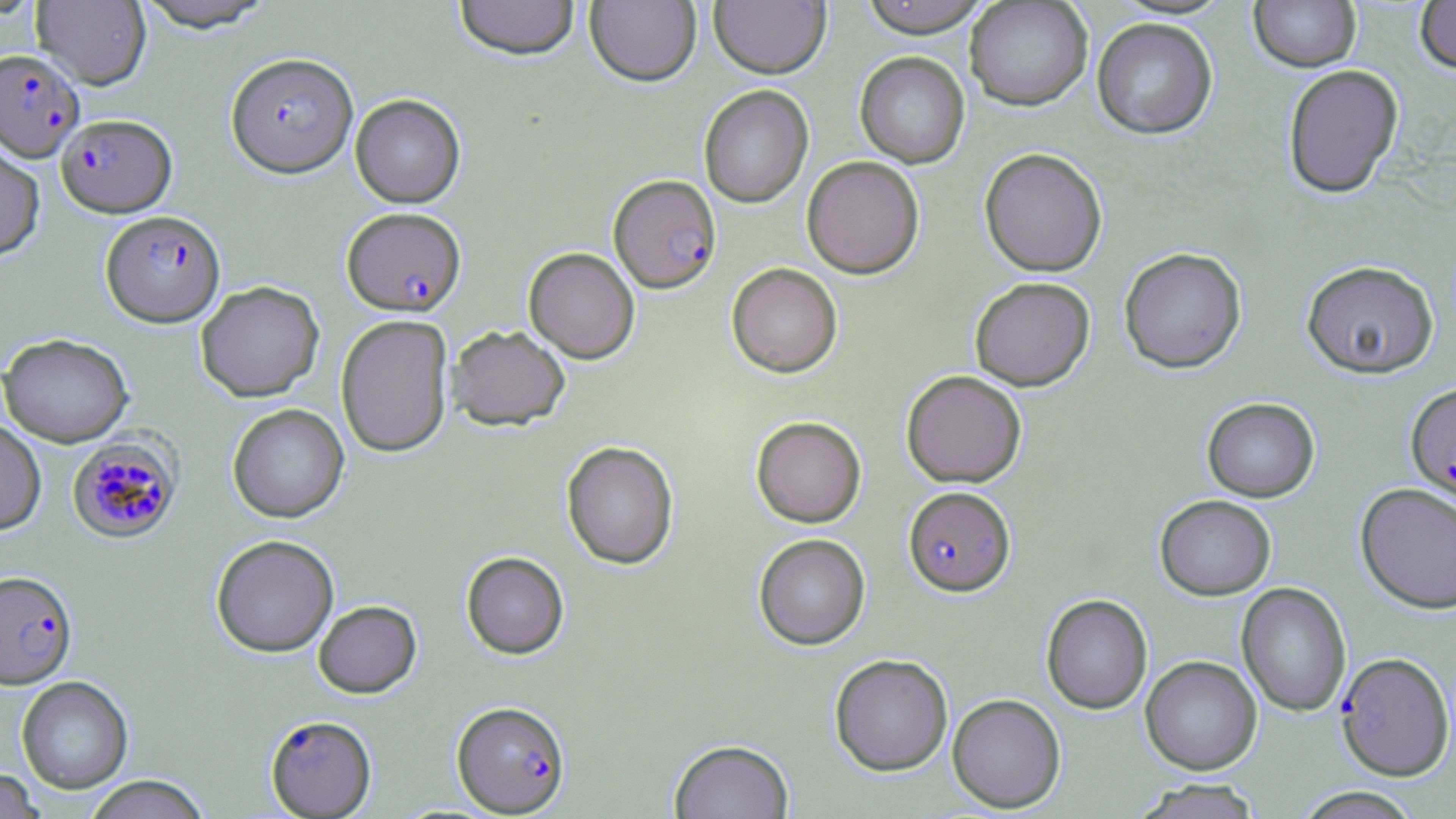

{
  "slide_level_diagnosis": "Plasmodium falciparum",
  "image_size": "1456×819 pixels",
  "preparation": "thin blood smear",
  "field_of_view": "single",
  "stain": "May-Grünwald-Giemsa",
  "magnification": "1000x",
  "uninfected_red_blood_cell_locations": "approximate bounding boxes as named x1/y1/x2/y2 corners in pixels: (x1=31, y1=0, x2=151, y2=90), (x1=132, y1=0, x2=276, y2=33), (x1=453, y1=0, x2=580, y2=63), (x1=585, y1=0, x2=701, y2=88), (x1=709, y1=0, x2=831, y2=80), (x1=858, y1=0, x2=991, y2=39), (x1=1414, y1=0, x2=1456, y2=77), (x1=964, y1=1, x2=1093, y2=113), (x1=1248, y1=1, x2=1361, y2=73), (x1=1091, y1=19, x2=1218, y2=141), (x1=855, y1=52, x2=970, y2=169), (x1=1282, y1=65, x2=1404, y2=199), (x1=698, y1=86, x2=814, y2=208), (x1=351, y1=94, x2=465, y2=208), (x1=0, y1=138, x2=45, y2=263), (x1=979, y1=149, x2=1108, y2=277), (x1=801, y1=157, x2=925, y2=279), (x1=523, y1=248, x2=639, y2=364), (x1=1119, y1=249, x2=1247, y2=376), (x1=1301, y1=262, x2=1439, y2=379), (x1=726, y1=264, x2=842, y2=378), (x1=969, y1=278, x2=1095, y2=392), (x1=195, y1=282, x2=325, y2=403), (x1=336, y1=314, x2=454, y2=459), (x1=447, y1=325, x2=570, y2=432), (x1=0, y1=335, x2=134, y2=447), (x1=901, y1=371, x2=1027, y2=488), (x1=1202, y1=398, x2=1320, y2=503), (x1=227, y1=404, x2=349, y2=524), (x1=751, y1=417, x2=866, y2=528), (x1=0, y1=421, x2=46, y2=536), (x1=561, y1=442, x2=679, y2=571), (x1=1355, y1=483, x2=1456, y2=615), (x1=1155, y1=496, x2=1276, y2=600), (x1=753, y1=534, x2=870, y2=651), (x1=211, y1=535, x2=339, y2=659), (x1=461, y1=552, x2=569, y2=661), (x1=1237, y1=583, x2=1351, y2=717), (x1=1041, y1=595, x2=1152, y2=714), (x1=313, y1=601, x2=422, y2=700), (x1=829, y1=654, x2=952, y2=777), (x1=1140, y1=656, x2=1262, y2=775), (x1=16, y1=677, x2=133, y2=794), (x1=947, y1=694, x2=1066, y2=813), (x1=668, y1=739, x2=794, y2=819), (x1=0, y1=768, x2=44, y2=819), (x1=83, y1=776, x2=211, y2=819), (x1=1132, y1=779, x2=1265, y2=818), (x1=1288, y1=786, x2=1426, y2=818)",
  "plasmodium_falciparum_infected_red_blood_cell_locations": "approximate bounding boxes as named x1/y1/x2/y2 corners in pixels: (x1=1, y1=49, x2=84, y2=162), (x1=225, y1=53, x2=357, y2=180), (x1=56, y1=115, x2=177, y2=218), (x1=608, y1=175, x2=721, y2=295), (x1=341, y1=207, x2=467, y2=318), (x1=100, y1=211, x2=226, y2=328), (x1=1405, y1=382, x2=1456, y2=509), (x1=67, y1=434, x2=184, y2=544), (x1=903, y1=487, x2=1016, y2=599), (x1=1, y1=571, x2=77, y2=690), (x1=1335, y1=653, x2=1454, y2=781), (x1=452, y1=702, x2=571, y2=817), (x1=264, y1=715, x2=376, y2=818)",
  "modality": "optical microscopy"
}